Point out each leukocyte.
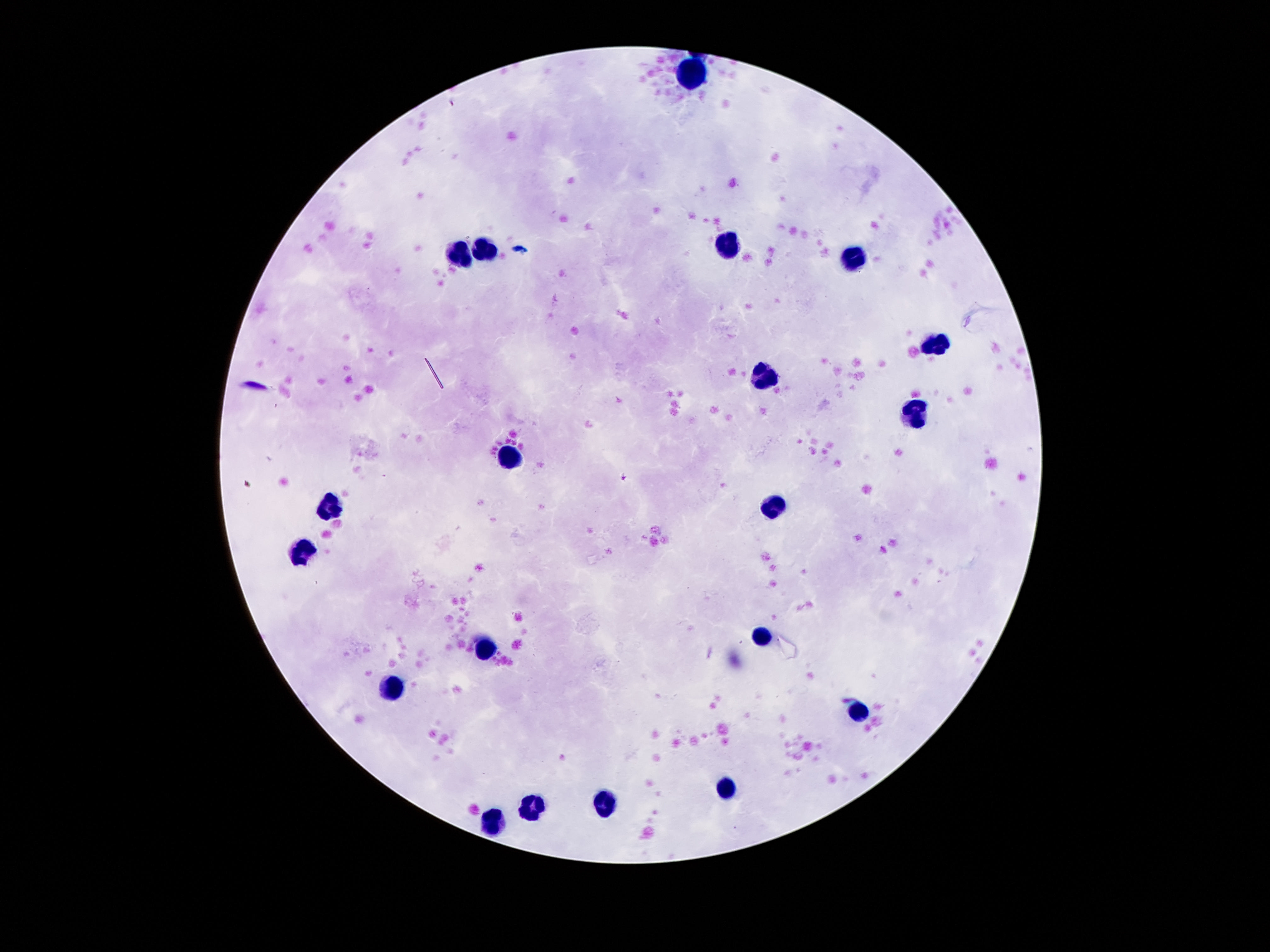
Approximate centers as {x, y} in pixels.
Leukocytes: {694, 76}, {725, 244}, {487, 247}, {460, 253}, {852, 259}, {938, 343}, {766, 378}, {913, 411}, {510, 454}, {776, 505}, {329, 509}, {299, 554}, {760, 635}, {487, 647}, {393, 688}, {858, 711}, {727, 789}, {604, 803}, {530, 807}, {489, 823}.

Summary:
  - Field of view: one from this slide
  - Preparation: thick blood film
  - Image size: 1270×952 pixels
  - Stain: Giemsa
  - Magnification: 100x
  - Capture: smartphone camera through the microscope eyepiece
  - Patient malaria status: uninfected